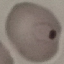

Malaria status: parasitized. Acquired by smartphone through the microscope eyepiece. Automatically extracted cell patch, resized to 64 × 64 pixels. Giemsa-stained preparation. Thin blood film.